Classify this cell by malaria status.
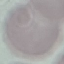
Uninfected.

Thin blood film. Acquired by smartphone through the microscope eyepiece. Giemsa stain. Automatically extracted cell patch, resized to 64 × 64 pixels.